Assess the morphology of the erythrocytes.
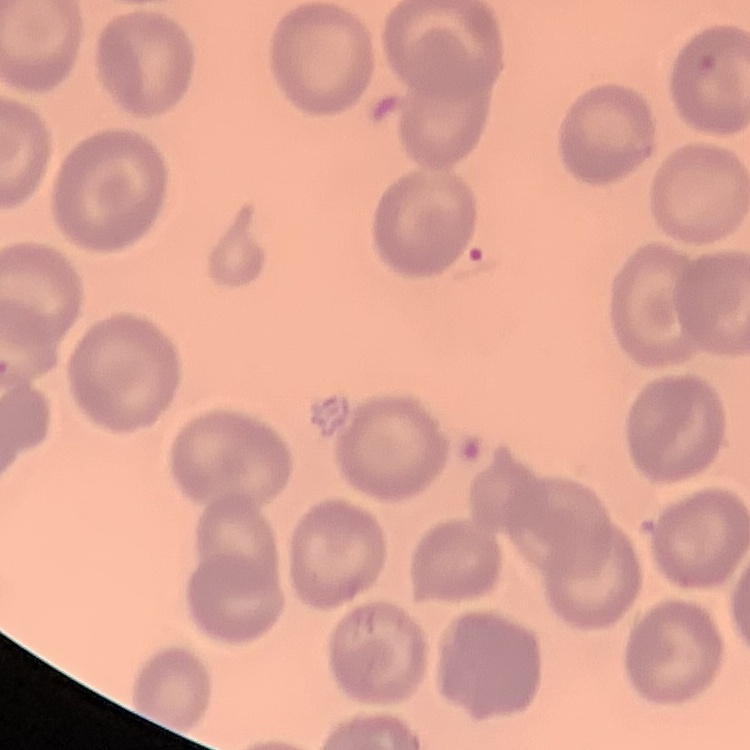

No rouleaux formation.

Thin blood film. Square crop of a larger photomicrograph. Field's or Giemsa stain.